State which parasite is depicted.
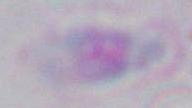

This is Toxoplasma gondii.

Summary:
  - Magnification: 1000x
  - Modality: photomicrograph